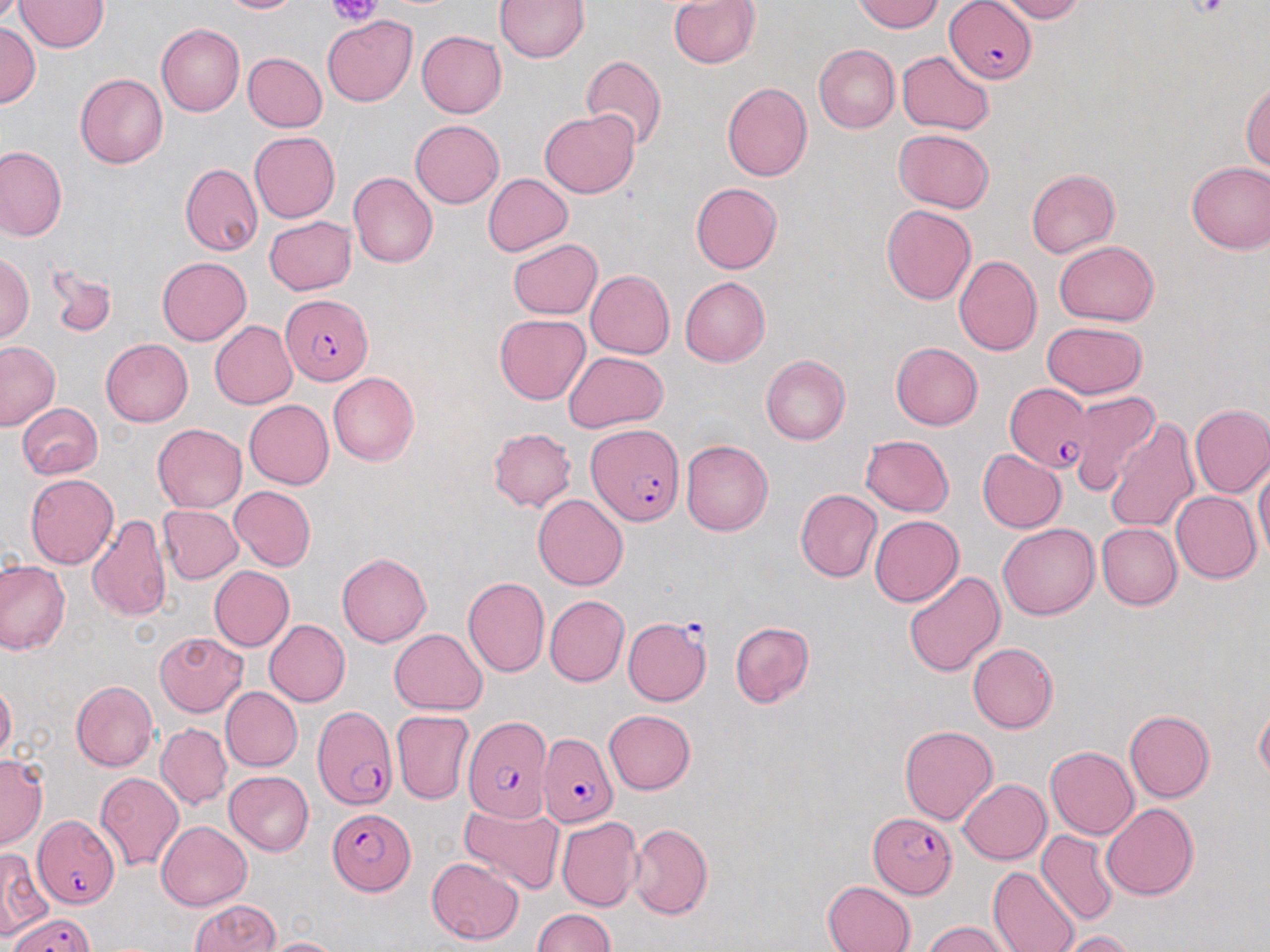

Plasmodium falciparum-infected red blood cell locations = approximate bounding boxes as (x1, y1, x2, y2) in pixels: (945, 1, 1038, 84), (280, 293, 373, 385), (1003, 384, 1094, 473), (585, 423, 684, 526), (623, 614, 713, 706), (313, 705, 398, 810), (462, 715, 553, 822), (537, 734, 617, 829), (327, 808, 414, 894), (869, 813, 956, 896), (32, 815, 119, 909), (10, 912, 96, 952)
slide-level diagnosis = Plasmodium falciparum
stain = May-Grünwald-Giemsa
magnification = 1000x
platelet locations = approximate bounding boxes as (x1, y1, x2, y2) in pixels: (325, 0, 383, 24), (1190, 0, 1230, 19)
modality = optical microscopy
preparation = thin blood smear
image size = 1270×952 pixels
field of view = single
uninfected red blood cell locations = approximate bounding boxes as (x1, y1, x2, y2) in pixels: (219, 0, 302, 14), (494, 0, 588, 61), (853, 0, 944, 32), (998, 0, 1083, 22), (15, 1, 107, 52), (669, 1, 761, 69), (322, 16, 417, 107), (0, 23, 41, 108), (155, 23, 244, 116), (416, 30, 507, 118), (814, 45, 900, 133), (897, 51, 993, 134), (243, 52, 327, 132), (581, 55, 667, 152), (75, 73, 167, 168), (721, 81, 812, 181), (1242, 81, 1270, 170), (540, 110, 640, 198), (410, 119, 504, 208), (893, 128, 994, 212), (249, 132, 340, 223), (0, 144, 66, 242), (1185, 160, 1269, 254), (180, 162, 262, 256), (1026, 169, 1119, 257), (348, 173, 437, 267), (482, 173, 573, 257), (690, 183, 782, 273), (881, 205, 976, 306), (264, 217, 357, 294), (507, 239, 603, 319), (1054, 240, 1159, 325), (0, 254, 33, 342), (953, 255, 1042, 356), (157, 257, 251, 345), (47, 263, 117, 339), (585, 270, 675, 358), (680, 277, 770, 367), (494, 313, 590, 405), (210, 321, 297, 408), (1041, 322, 1149, 399), (101, 338, 193, 426), (0, 340, 60, 431), (891, 342, 983, 430), (562, 351, 667, 433), (760, 355, 850, 445), (328, 372, 419, 466), (1067, 390, 1158, 496), (244, 399, 334, 488), (18, 403, 103, 479), (1189, 403, 1270, 498), (1105, 416, 1198, 534), (153, 423, 246, 512), (487, 428, 577, 511), (860, 434, 954, 516), (681, 440, 773, 536), (977, 448, 1065, 533), (1254, 464, 1270, 561), (25, 474, 119, 569), (229, 485, 315, 571), (795, 489, 881, 581), (1170, 490, 1261, 583), (532, 494, 629, 591), (158, 504, 243, 583), (88, 513, 172, 622), (870, 515, 963, 606), (997, 524, 1099, 619), (1097, 524, 1181, 610), (337, 553, 432, 646), (0, 558, 70, 655), (210, 566, 294, 651), (905, 570, 1005, 677), (462, 577, 549, 677), (544, 594, 630, 687), (264, 619, 350, 706), (729, 621, 815, 707), (390, 628, 488, 714), (156, 632, 248, 716), (968, 643, 1058, 733), (71, 680, 158, 771), (0, 681, 16, 764), (220, 687, 302, 771), (1254, 701, 1270, 784), (604, 709, 696, 794), (392, 710, 473, 804), (1124, 710, 1215, 802), (156, 723, 232, 809), (899, 725, 998, 825), (1044, 746, 1138, 839), (0, 755, 47, 849), (225, 771, 314, 856), (95, 772, 184, 871), (958, 779, 1051, 864), (1102, 803, 1198, 901), (460, 804, 565, 895), (557, 816, 642, 912), (1038, 819, 1189, 916), (157, 821, 251, 910), (628, 823, 713, 920), (1036, 830, 1119, 926), (0, 850, 51, 941), (426, 857, 524, 944), (988, 867, 1080, 952), (822, 881, 915, 952), (189, 899, 279, 951), (533, 908, 616, 951), (923, 921, 1012, 952), (1056, 929, 1140, 952), (259, 936, 346, 951)